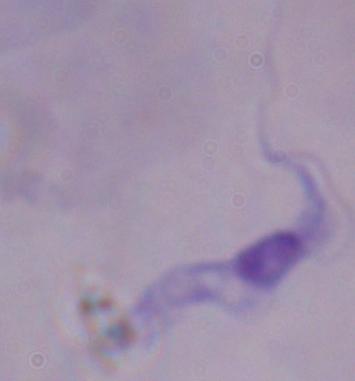
{
  "modality": "photomicrograph",
  "magnification": "1000x",
  "identification": "trypanosome"
}